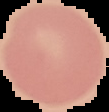

image size = 109×112 pixels
image type = segmented cell region with the area outside set to black
result = negative for malaria parasites
preparation = thin blood film